Locate every blood parasite and identify its species.
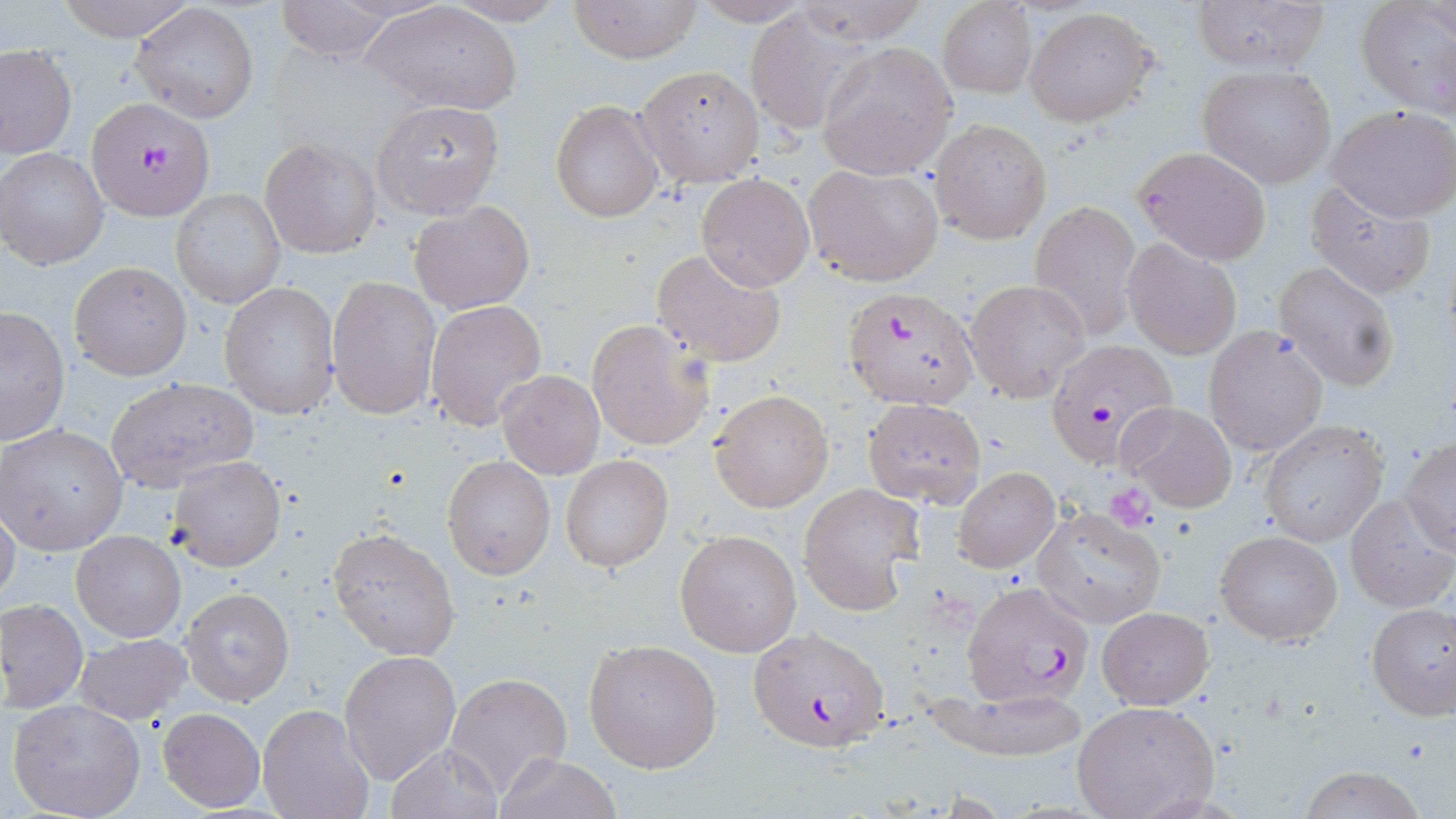
Approximate bounding boxes as named x1/y1/x2/y2 corners in pixels.
Plasmodium falciparum-infected red blood cells: (x1=91, y1=109, x2=215, y2=231), (x1=842, y1=284, x2=982, y2=411), (x1=1044, y1=340, x2=1177, y2=469), (x1=962, y1=581, x2=1097, y2=710), (x1=747, y1=628, x2=893, y2=753).
No Plasmodium ovale, Plasmodium malariae, Plasmodium vivax, Babesia divergens, or Trypanosoma brucei observed.

slide-level diagnosis = Plasmodium falciparum
field of view = single
uninfected red blood cell locations = approximate bounding boxes as named x1/y1/x2/y2 corners in pixels: (x1=51, y1=0, x2=201, y2=43), (x1=274, y1=0, x2=405, y2=57), (x1=362, y1=0, x2=522, y2=115), (x1=436, y1=0, x2=572, y2=25), (x1=569, y1=0, x2=700, y2=63), (x1=689, y1=0, x2=818, y2=25), (x1=793, y1=0, x2=931, y2=47), (x1=1190, y1=0, x2=1329, y2=74), (x1=937, y1=1, x2=1038, y2=98), (x1=1356, y1=3, x2=1455, y2=119), (x1=131, y1=4, x2=258, y2=122), (x1=1024, y1=7, x2=1157, y2=126), (x1=741, y1=10, x2=862, y2=135), (x1=817, y1=41, x2=959, y2=180), (x1=1, y1=46, x2=76, y2=160), (x1=1198, y1=63, x2=1337, y2=188), (x1=635, y1=65, x2=764, y2=188), (x1=372, y1=100, x2=507, y2=218), (x1=551, y1=100, x2=664, y2=223), (x1=1327, y1=103, x2=1455, y2=222), (x1=929, y1=117, x2=1053, y2=244), (x1=260, y1=137, x2=380, y2=260), (x1=1132, y1=145, x2=1273, y2=265), (x1=1, y1=148, x2=108, y2=270), (x1=803, y1=164, x2=943, y2=285), (x1=697, y1=174, x2=814, y2=290), (x1=1307, y1=182, x2=1437, y2=300), (x1=170, y1=189, x2=285, y2=309), (x1=1030, y1=200, x2=1142, y2=340), (x1=409, y1=201, x2=535, y2=315), (x1=1122, y1=239, x2=1241, y2=358), (x1=651, y1=248, x2=787, y2=369), (x1=69, y1=261, x2=191, y2=381), (x1=1274, y1=261, x2=1401, y2=392), (x1=327, y1=275, x2=442, y2=419), (x1=963, y1=279, x2=1092, y2=402), (x1=218, y1=283, x2=339, y2=418), (x1=424, y1=300, x2=547, y2=431), (x1=0, y1=307, x2=71, y2=447), (x1=585, y1=319, x2=715, y2=451), (x1=1203, y1=326, x2=1329, y2=457), (x1=496, y1=369, x2=605, y2=479), (x1=105, y1=376, x2=259, y2=491), (x1=709, y1=389, x2=834, y2=513), (x1=861, y1=398, x2=987, y2=507), (x1=1116, y1=401, x2=1238, y2=512), (x1=1259, y1=419, x2=1390, y2=546), (x1=1, y1=424, x2=128, y2=556), (x1=1400, y1=438, x2=1455, y2=554), (x1=442, y1=455, x2=556, y2=581), (x1=559, y1=455, x2=674, y2=573), (x1=168, y1=456, x2=285, y2=572), (x1=954, y1=467, x2=1059, y2=572), (x1=798, y1=484, x2=922, y2=615), (x1=1344, y1=494, x2=1454, y2=612), (x1=0, y1=501, x2=21, y2=613), (x1=1032, y1=505, x2=1165, y2=628), (x1=327, y1=528, x2=460, y2=661), (x1=674, y1=528, x2=802, y2=657), (x1=1215, y1=529, x2=1343, y2=645), (x1=72, y1=531, x2=186, y2=642), (x1=181, y1=587, x2=294, y2=706), (x1=1, y1=598, x2=88, y2=714), (x1=1365, y1=603, x2=1456, y2=720), (x1=1098, y1=607, x2=1213, y2=709), (x1=75, y1=633, x2=191, y2=724), (x1=584, y1=638, x2=723, y2=773), (x1=339, y1=649, x2=461, y2=783), (x1=445, y1=671, x2=573, y2=797), (x1=919, y1=686, x2=1091, y2=759), (x1=8, y1=698, x2=147, y2=819), (x1=1071, y1=700, x2=1220, y2=819), (x1=257, y1=703, x2=375, y2=819), (x1=157, y1=708, x2=267, y2=811), (x1=387, y1=743, x2=504, y2=819), (x1=496, y1=753, x2=622, y2=819), (x1=1297, y1=764, x2=1430, y2=819)
modality = light microscopy
stain = May-Grünwald-Giemsa
magnification = 1000x
platelet locations = approximate bounding boxes as named x1/y1/x2/y2 corners in pixels: (x1=1105, y1=483, x2=1158, y2=528)
image size = 1456×819 pixels
preparation = thin blood smear